Classify this cell by malaria status.
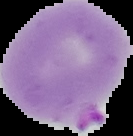

It is parasitized.

Cell region segmented out of the field of view; the surrounding area is masked to black. Image is 133×136 pixels. From a thin blood film.